Locate every Plasmodium ovale-infected red blood cell.
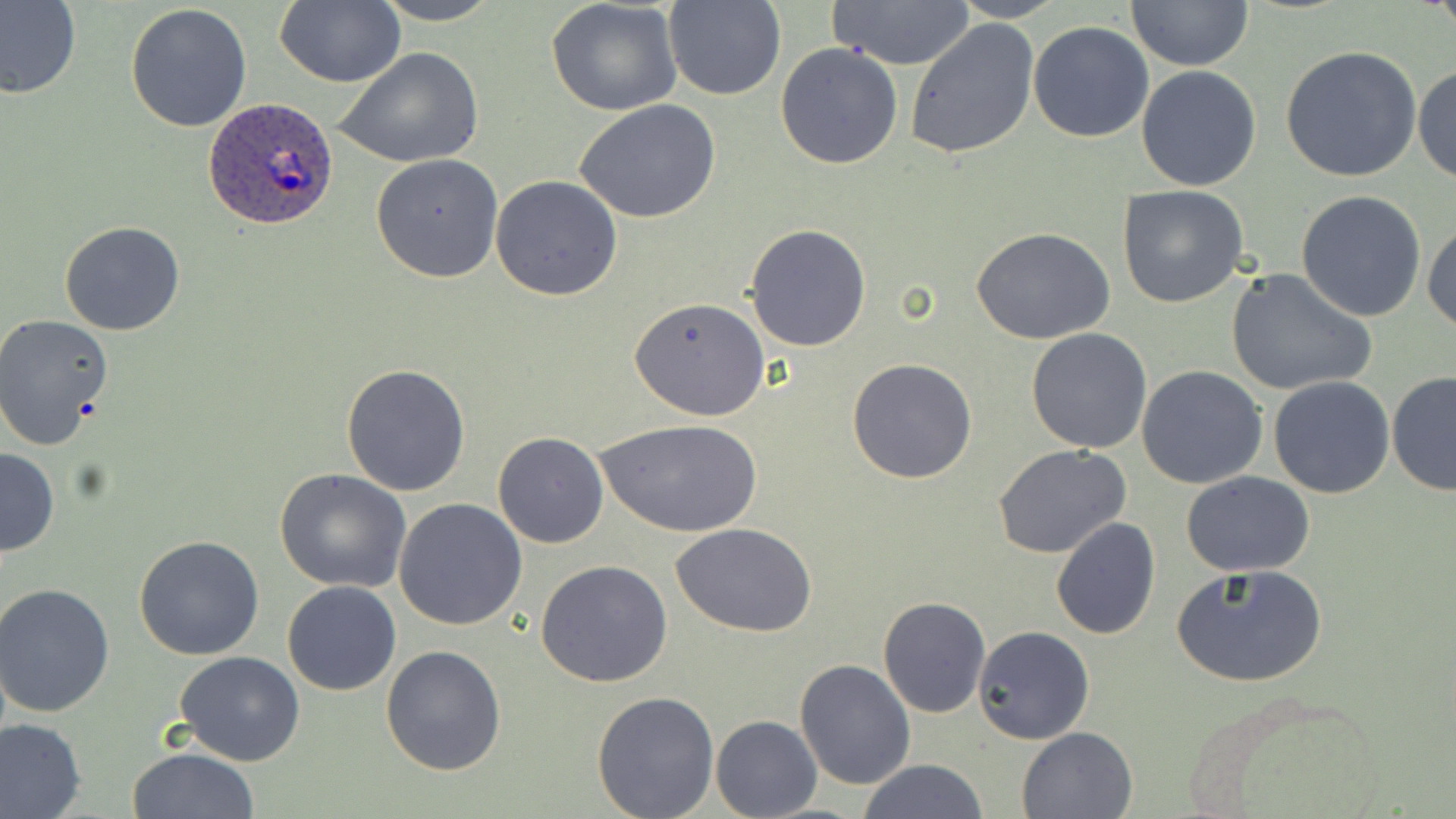

Approximate bounding boxes as (x1,y1)-(x2,y2) corner pairs in pixels.
Plasmodium ovale-infected red blood cells: (203,99)-(341,229).

Summary:
  - Uninfected red blood cell locations: (0,0)-(82,101), (275,0)-(403,87), (372,0)-(502,25), (662,0)-(784,101), (947,0)-(1068,22), (829,1)-(975,70), (1127,1)-(1253,71), (546,2)-(684,117), (125,5)-(253,132), (1028,19)-(1154,142), (906,20)-(1038,160), (775,41)-(905,170), (1278,44)-(1424,182), (337,49)-(484,168), (1413,65)-(1455,186), (1135,66)-(1261,191), (574,99)-(720,224), (371,154)-(504,283), (490,175)-(622,300), (1118,184)-(1250,308), (1295,190)-(1427,323), (1423,218)-(1455,335), (59,220)-(186,335), (744,225)-(871,350), (972,227)-(1115,346), (1227,268)-(1376,398), (629,296)-(770,421), (2,314)-(117,452), (1025,328)-(1152,454), (847,357)-(978,484), (341,364)-(471,497), (1137,366)-(1268,489), (1386,371)-(1456,495), (1268,375)-(1397,498), (597,418)-(762,539), (493,431)-(610,548), (993,445)-(1133,561), (0,447)-(59,559), (276,468)-(411,591), (1181,471)-(1316,578), (394,497)-(527,631), (1050,518)-(1161,640), (674,525)-(817,637), (134,534)-(266,661), (535,560)-(675,686), (1172,562)-(1329,689), (282,580)-(401,695), (1,584)-(118,719), (877,596)-(990,718), (972,626)-(1095,744), (380,645)-(508,776), (173,650)-(306,766), (795,659)-(915,791), (590,691)-(720,819), (711,715)-(822,819), (0,717)-(86,818), (1017,727)-(1137,818), (127,747)-(259,819), (859,759)-(988,819)
  - Slide-level diagnosis: Plasmodium ovale
  - Modality: light microscopy
  - Image size: 1456×819 pixels
  - Preparation: thin blood smear
  - Field of view: one of a larger specimen
  - Magnification: 1000x
  - Stain: May-Grünwald-Giemsa